Assess this cell for malaria.
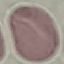
Uninfected.

Thin smear of blood. Cell patch, automatically extracted from a larger field of view and resized to 64 × 64 pixels. Photographed with a smartphone camera at the microscope eyepiece. Giemsa-stained preparation.